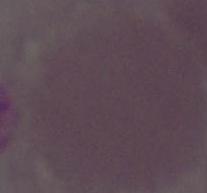
Summary:
  - Modality: photomicrograph
  - Magnification: 1000x
  - Identification: erythrocyte